Describe the morphology of the erythrocytes.
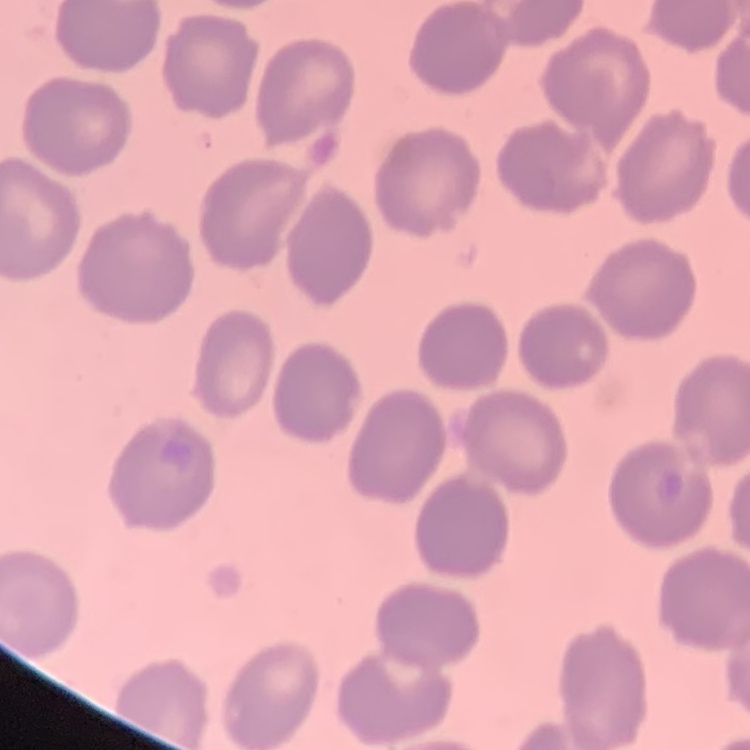

No rouleaux formation.

Summary:
  - Image type: square crop of a larger photomicrograph
  - Preparation: thin blood smear
  - Stain: Field's or Giemsa